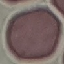
Summary:
  - Malaria status: uninfected
  - Preparation: thin blood film
  - Stain: Giemsa
  - Image type: cell patch, automatically extracted from a larger field of view and resized to 64 × 64 pixels
  - Capture: smartphone camera at the microscope eyepiece